Report the malaria status of this cell.
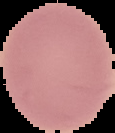

Uninfected.

Summary:
  - Image type: segmented cell region on a black background
  - Preparation: thin blood film
  - Image size: 115×133 pixels